Report the malaria status of this cell.
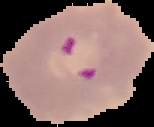
Parasitized.

{
  "preparation": "thin blood film",
  "image_type": "segmented cell region with the area outside set to black",
  "image_size": "154×127 pixels"
}